Name the blood parasite species.
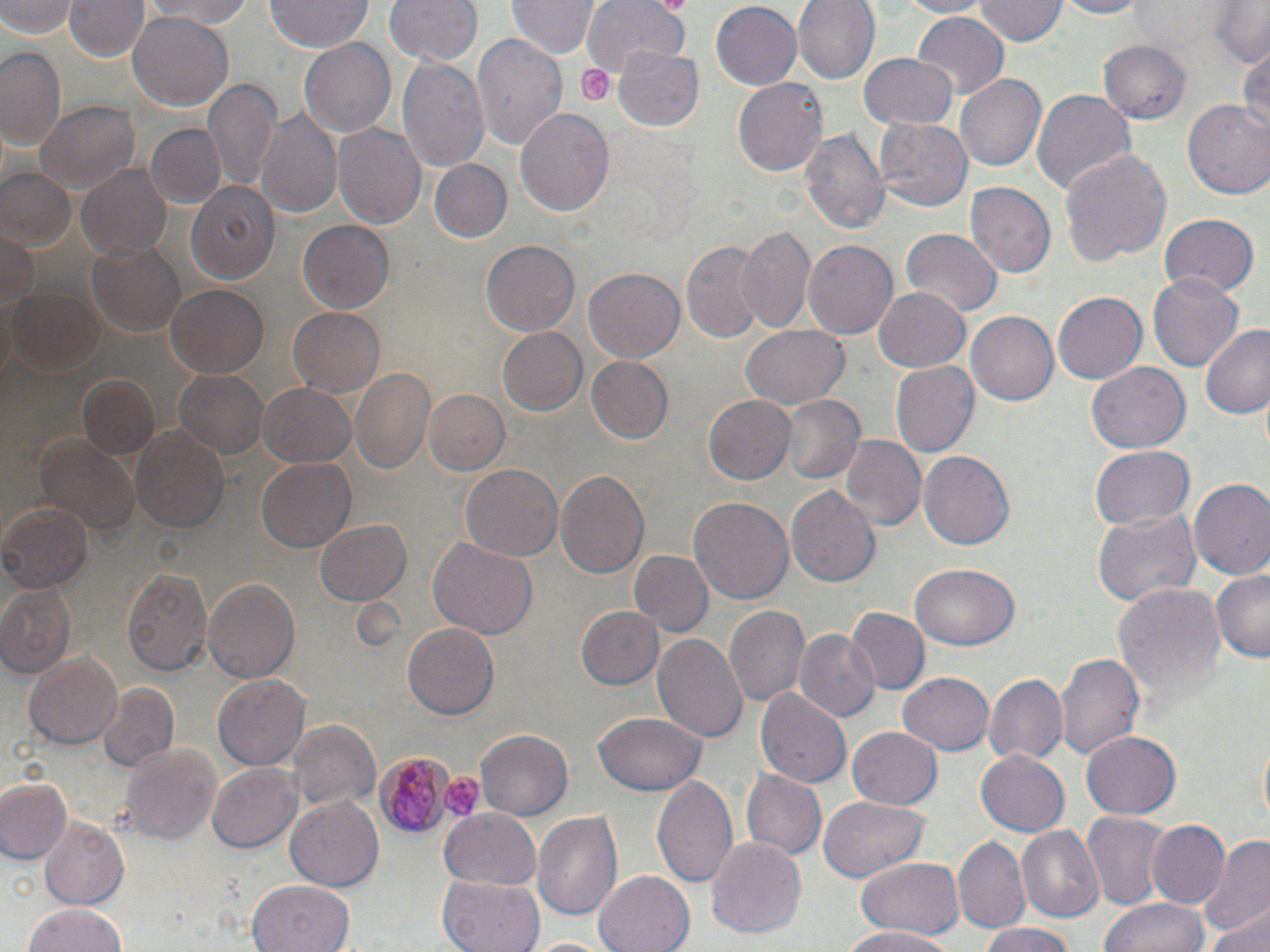
Plasmodium malariae.

Approximate bounding boxes as named x1/y1/x2/y2 corners in pixels. Platelet locations: (x1=576, y1=63, x2=612, y2=107), (x1=439, y1=775, x2=483, y2=822). Uninfected red blood cell locations: (x1=1, y1=0, x2=77, y2=39), (x1=66, y1=0, x2=148, y2=63), (x1=385, y1=0, x2=482, y2=67), (x1=508, y1=0, x2=598, y2=60), (x1=582, y1=0, x2=689, y2=74), (x1=709, y1=0, x2=801, y2=88), (x1=792, y1=0, x2=877, y2=85), (x1=891, y1=0, x2=994, y2=17), (x1=974, y1=0, x2=1065, y2=46), (x1=1052, y1=0, x2=1150, y2=19), (x1=1208, y1=0, x2=1270, y2=69), (x1=137, y1=1, x2=265, y2=27), (x1=265, y1=1, x2=372, y2=53), (x1=912, y1=11, x2=1008, y2=100), (x1=127, y1=12, x2=233, y2=110), (x1=471, y1=34, x2=569, y2=154), (x1=299, y1=38, x2=398, y2=136), (x1=1098, y1=41, x2=1190, y2=122), (x1=0, y1=45, x2=65, y2=150), (x1=616, y1=46, x2=703, y2=130), (x1=1236, y1=46, x2=1269, y2=138), (x1=859, y1=53, x2=959, y2=132), (x1=397, y1=58, x2=489, y2=172), (x1=956, y1=73, x2=1047, y2=171), (x1=732, y1=76, x2=828, y2=178), (x1=206, y1=78, x2=281, y2=193), (x1=1030, y1=86, x2=1135, y2=197), (x1=35, y1=100, x2=138, y2=194), (x1=1184, y1=101, x2=1270, y2=200), (x1=515, y1=106, x2=614, y2=218), (x1=256, y1=109, x2=341, y2=222), (x1=875, y1=117, x2=973, y2=211), (x1=145, y1=122, x2=224, y2=209), (x1=333, y1=124, x2=425, y2=228), (x1=801, y1=126, x2=889, y2=241), (x1=1059, y1=147, x2=1171, y2=263), (x1=75, y1=159, x2=175, y2=260), (x1=427, y1=159, x2=512, y2=243), (x1=1, y1=168, x2=76, y2=247), (x1=185, y1=182, x2=279, y2=286), (x1=964, y1=183, x2=1054, y2=279), (x1=1158, y1=213, x2=1260, y2=298), (x1=296, y1=219, x2=395, y2=314), (x1=736, y1=226, x2=816, y2=336), (x1=0, y1=228, x2=38, y2=317), (x1=901, y1=230, x2=1001, y2=316), (x1=803, y1=238, x2=898, y2=339), (x1=680, y1=239, x2=765, y2=344), (x1=86, y1=240, x2=185, y2=337), (x1=481, y1=240, x2=580, y2=336), (x1=582, y1=266, x2=685, y2=363), (x1=1149, y1=272, x2=1244, y2=373), (x1=164, y1=286, x2=268, y2=378), (x1=872, y1=286, x2=972, y2=372), (x1=8, y1=287, x2=106, y2=378), (x1=1053, y1=290, x2=1147, y2=384), (x1=289, y1=306, x2=384, y2=395), (x1=966, y1=311, x2=1061, y2=405), (x1=1198, y1=324, x2=1270, y2=420), (x1=739, y1=325, x2=850, y2=412), (x1=497, y1=326, x2=587, y2=416), (x1=584, y1=355, x2=673, y2=444), (x1=890, y1=361, x2=978, y2=458), (x1=1086, y1=361, x2=1190, y2=454), (x1=350, y1=366, x2=436, y2=477), (x1=173, y1=367, x2=271, y2=461), (x1=76, y1=376, x2=162, y2=463), (x1=257, y1=382, x2=357, y2=468), (x1=422, y1=389, x2=510, y2=476), (x1=704, y1=394, x2=794, y2=485), (x1=781, y1=395, x2=864, y2=485), (x1=131, y1=426, x2=230, y2=534), (x1=35, y1=434, x2=141, y2=540), (x1=838, y1=436, x2=925, y2=535), (x1=1089, y1=445, x2=1195, y2=530), (x1=918, y1=451, x2=1013, y2=551), (x1=257, y1=456, x2=356, y2=554), (x1=460, y1=463, x2=563, y2=561), (x1=555, y1=470, x2=650, y2=579), (x1=1188, y1=480, x2=1270, y2=583), (x1=786, y1=484, x2=881, y2=590), (x1=688, y1=495, x2=792, y2=608), (x1=0, y1=502, x2=93, y2=596), (x1=1092, y1=507, x2=1199, y2=609), (x1=314, y1=519, x2=411, y2=607), (x1=428, y1=536, x2=539, y2=639), (x1=631, y1=550, x2=711, y2=636), (x1=911, y1=564, x2=1018, y2=651), (x1=121, y1=565, x2=211, y2=679), (x1=1211, y1=568, x2=1270, y2=662), (x1=201, y1=579, x2=299, y2=686), (x1=1112, y1=583, x2=1224, y2=706), (x1=1, y1=584, x2=75, y2=675), (x1=576, y1=606, x2=663, y2=691), (x1=724, y1=606, x2=810, y2=709), (x1=850, y1=608, x2=930, y2=694), (x1=737, y1=618, x2=870, y2=715), (x1=402, y1=623, x2=499, y2=721), (x1=794, y1=629, x2=881, y2=722), (x1=653, y1=631, x2=747, y2=744), (x1=26, y1=651, x2=123, y2=750), (x1=1056, y1=652, x2=1146, y2=764), (x1=897, y1=669, x2=993, y2=753), (x1=213, y1=673, x2=309, y2=770), (x1=984, y1=674, x2=1067, y2=765), (x1=96, y1=683, x2=178, y2=773), (x1=756, y1=687, x2=851, y2=791), (x1=593, y1=711, x2=706, y2=795), (x1=289, y1=720, x2=380, y2=812), (x1=846, y1=726, x2=944, y2=811), (x1=475, y1=731, x2=572, y2=820), (x1=1082, y1=731, x2=1181, y2=818), (x1=119, y1=742, x2=222, y2=847), (x1=975, y1=750, x2=1070, y2=837), (x1=208, y1=762, x2=300, y2=852), (x1=740, y1=770, x2=826, y2=864), (x1=651, y1=775, x2=739, y2=891), (x1=0, y1=778, x2=70, y2=863), (x1=818, y1=797, x2=929, y2=881), (x1=286, y1=798, x2=382, y2=889), (x1=440, y1=807, x2=542, y2=889), (x1=532, y1=807, x2=625, y2=925), (x1=1082, y1=813, x2=1173, y2=913), (x1=39, y1=817, x2=129, y2=911), (x1=1146, y1=818, x2=1230, y2=911), (x1=1016, y1=827, x2=1103, y2=922), (x1=1198, y1=833, x2=1270, y2=939), (x1=707, y1=835, x2=806, y2=940), (x1=953, y1=836, x2=1031, y2=935), (x1=854, y1=857, x2=964, y2=941), (x1=593, y1=871, x2=694, y2=952), (x1=439, y1=873, x2=545, y2=952), (x1=248, y1=879, x2=357, y2=952), (x1=1100, y1=897, x2=1209, y2=952), (x1=23, y1=900, x2=128, y2=952), (x1=1208, y1=904, x2=1270, y2=952), (x1=977, y1=923, x2=1076, y2=952), (x1=839, y1=926, x2=956, y2=952), (x1=526, y1=935, x2=616, y2=952). Plasmodium malariae-infected red blood cell locations: (x1=372, y1=748, x2=459, y2=838). Light microscopy. One field of a larger specimen. Image is 1270×952 pixels. Thin blood smear. 1000x magnification. May-Grünwald-Giemsa stain.